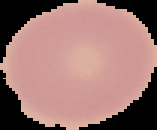

malaria_status: uninfected
image_type: segmented cell region on a black background
image_size: 157×130 pixels
preparation: thin blood film